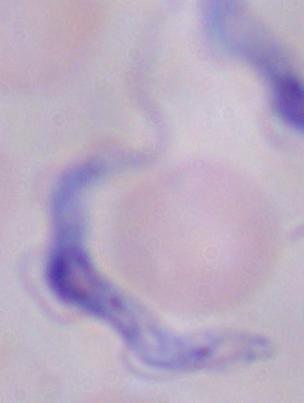

Micrograph. Captured at 1000x magnification. A trypanosome is shown.